State which cell type is depicted.
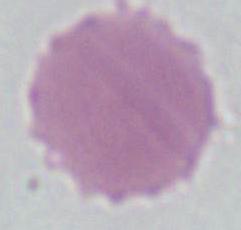

This is an erythrocyte.

{
  "magnification": "1000x",
  "modality": "photomicrograph"
}